Identify the parasite.
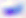

This is Toxoplasma gondii.

Photomicrograph. 400x magnification.